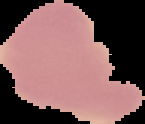
image size = 145×124 pixels
image type = cell region segmented out of the field of view; surrounding area masked to black
malaria status = uninfected
preparation = thin blood smear